Identify the parasite.
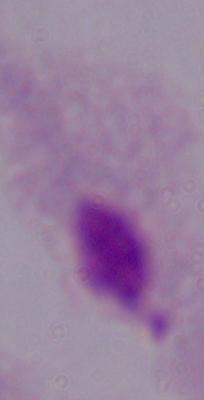
This is a trichomonad.

Summary:
  - Modality: micrograph
  - Magnification: 1000x